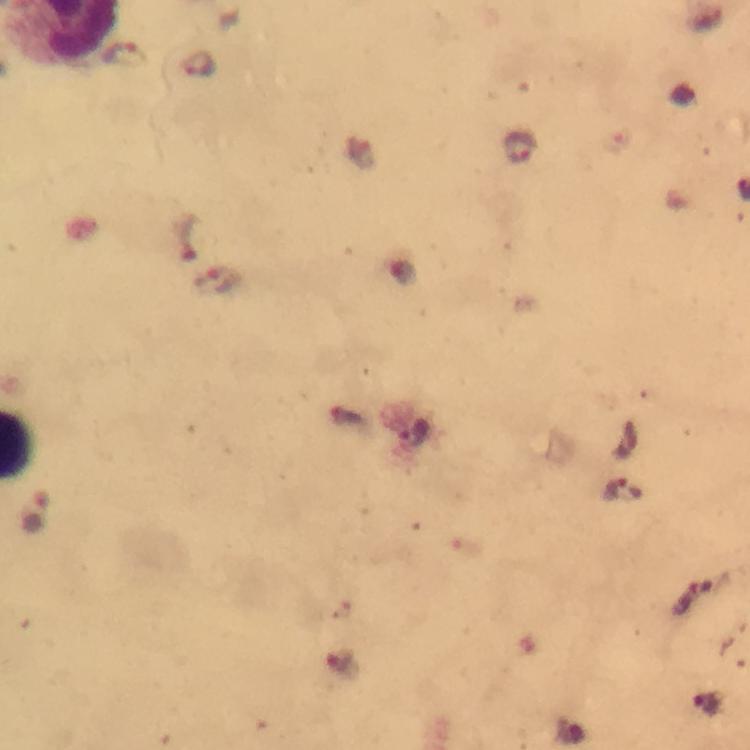

Approximate centers as [x, y] in pixels. Plasmodium parasite locations: [124, 55], [200, 66], [520, 146], [621, 492]. Immersion oil was used. Smartphone photograph taken through a microscope. Cropped region of a single field of view. Giemsa stain. Image is 750×750 pixels. At 100x magnification. Thick blood film. From a diagnostic examination for malaria.